Report the malaria status of this cell.
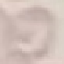

Uninfected.

Summary:
  - Preparation: thin smear
  - Capture: smartphone through the microscope eyepiece
  - Image type: cell patch, automatically extracted from a larger field of view and resized to 64 × 64 pixels
  - Stain: Giemsa